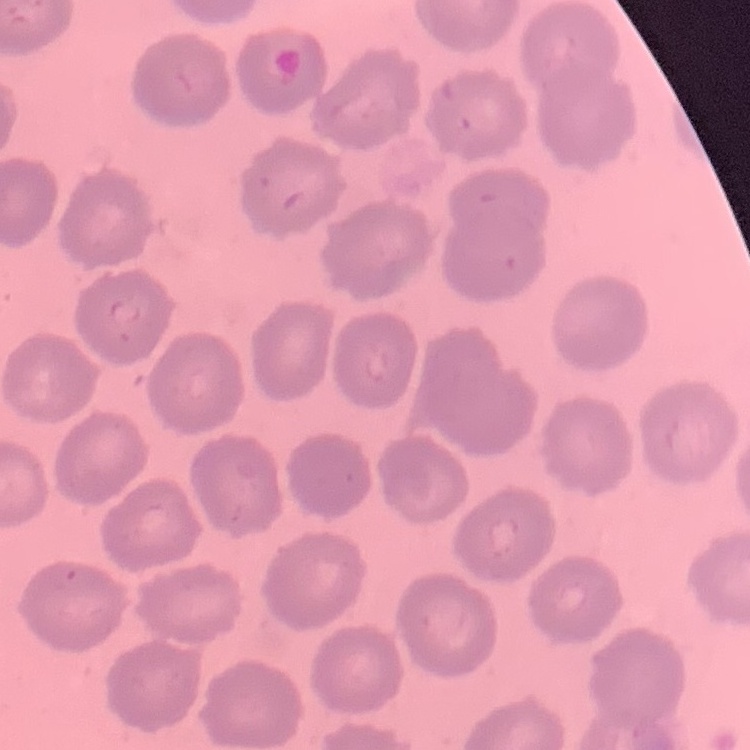
Summary:
  - Erythrocyte morphology: no rouleaux formation
  - Stain: Field's or Giemsa
  - Preparation: thin blood smear
  - Image type: one tile cut from a larger photomicrograph